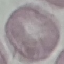

Summary:
  - Malaria status: uninfected
  - Capture: smartphone camera at the microscope eyepiece
  - Preparation: thin blood film
  - Stain: Giemsa
  - Image type: cell patch, automatically extracted from a larger field of view and resized to 64 × 64 pixels